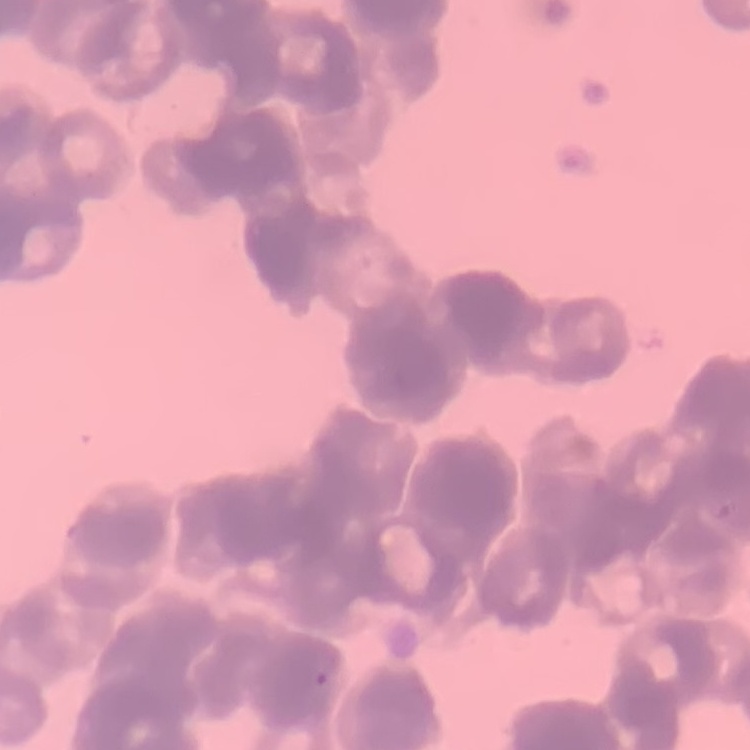

The erythrocytes show rouleaux formation. Square crop of a larger photomicrograph. Stained with either Field's or Giemsa. Thin blood film.